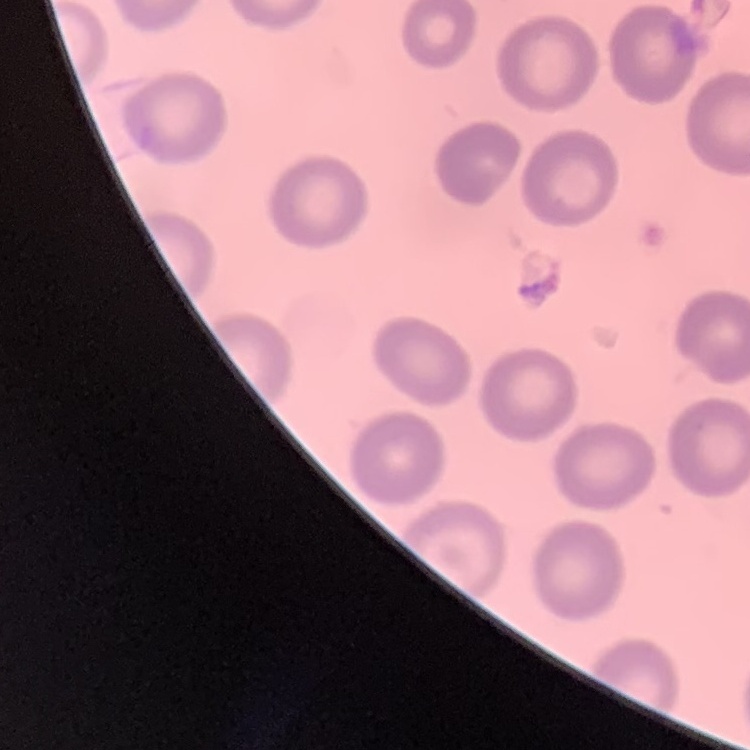 The erythrocytes exhibit no rouleaux formation. One tile cut from a larger photomicrograph. Field's or Giemsa stain. Thin blood film.